Describe the morphology of the erythrocytes.
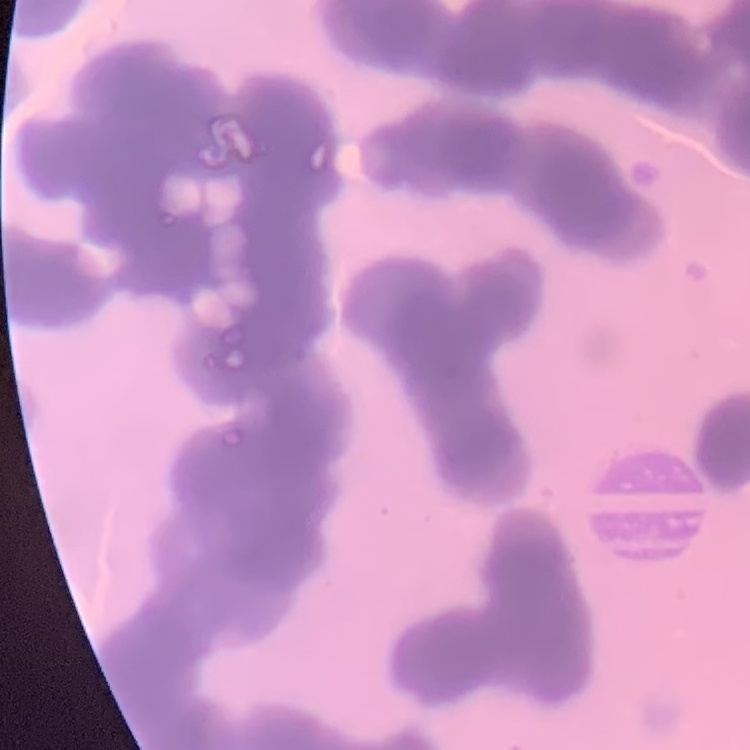
They show rouleaux formation.

image type = square crop of a larger photomicrograph
stain = Field's or Giemsa
preparation = thin blood film